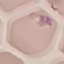

{
  "malaria_status": "uninfected",
  "stain": "Giemsa",
  "capture": "smartphone through the microscope eyepiece",
  "image_type": "cell patch, automatically extracted from a larger field of view and resized to 64 × 64 pixels",
  "preparation": "thin blood smear"
}